Give the position of every Plasmodium parasite.
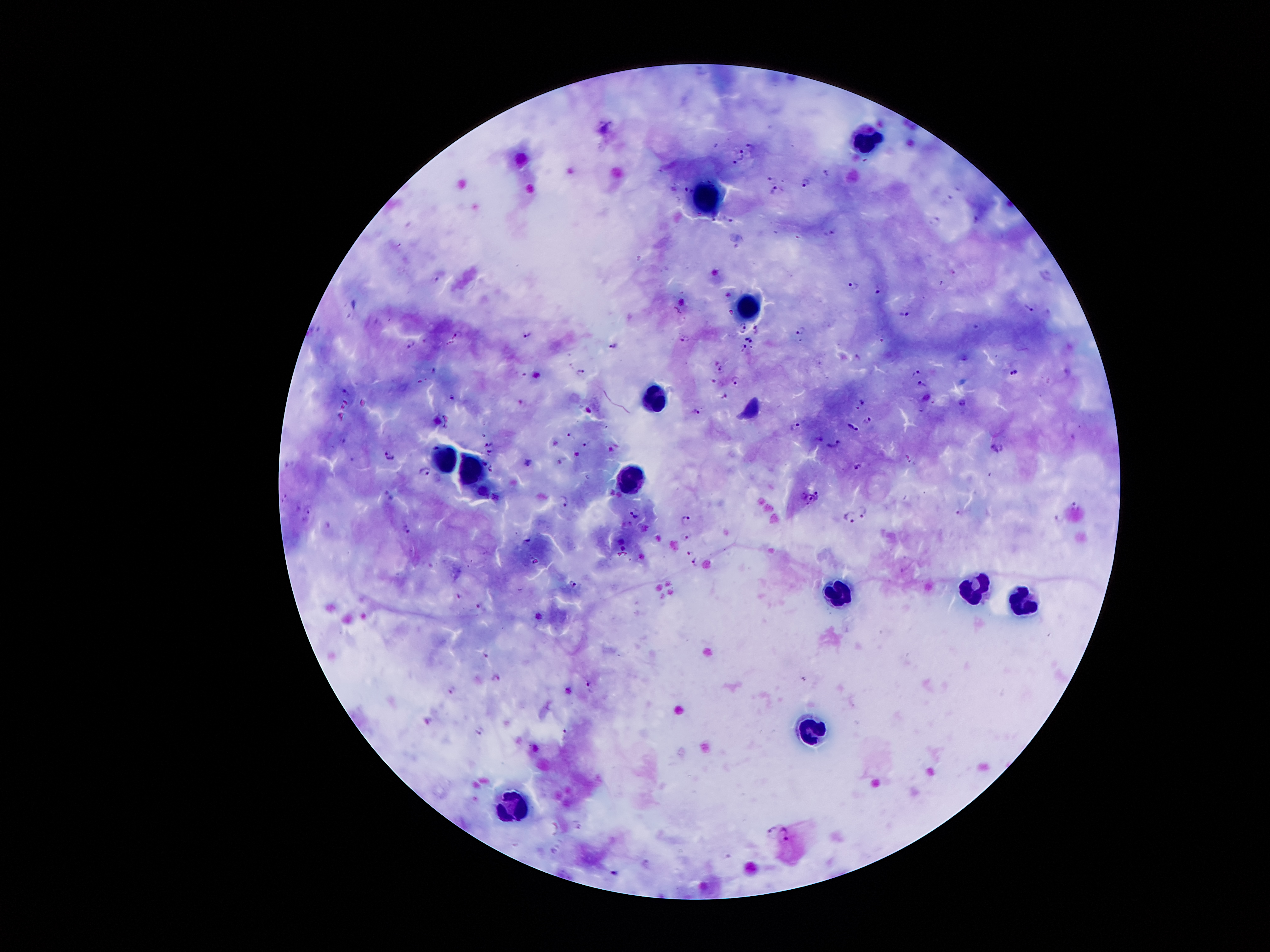

Approximate centers as [x, y] in pixels.
Plasmodium parasites: [750, 146], [739, 150], [739, 158], [827, 174], [772, 177], [804, 183], [686, 189], [776, 191], [729, 219], [935, 221], [829, 233], [435, 277], [853, 284], [880, 290], [1030, 310], [906, 315], [742, 327], [755, 328], [798, 330], [528, 333], [456, 334], [684, 338], [749, 339], [412, 344], [612, 344], [742, 345], [857, 357], [718, 366], [435, 370], [1013, 371], [915, 372], [581, 373], [715, 380], [735, 380], [922, 384], [344, 391], [453, 396], [727, 397], [961, 402], [862, 403], [695, 409], [867, 420], [795, 426], [853, 426], [571, 435], [342, 439], [586, 442], [490, 443], [834, 443], [996, 448], [489, 451], [389, 455], [528, 461], [483, 462], [857, 466], [490, 468], [425, 470], [817, 494], [389, 495], [804, 495], [811, 497], [284, 499], [564, 500], [1077, 506], [863, 510], [308, 511], [960, 511], [633, 513], [851, 516], [685, 520], [405, 528], [685, 537], [525, 540], [689, 551], [696, 561], [573, 584], [459, 595], [480, 606], [486, 654], [496, 676], [589, 685], [453, 688], [770, 828], [784, 834].

Leukocyte locations: [868, 147], [706, 193], [745, 304], [652, 397], [444, 453], [468, 467], [628, 475], [840, 589], [972, 590], [1027, 600], [811, 724], [512, 814]. Single field of view. Thick blood film. Image is 1270×952 pixels. Smartphone photograph taken through the microscope eyepiece. Giemsa stain. Patient malaria status: infected with Plasmodium falciparum. 100x magnification.